State which cell type is depicted.
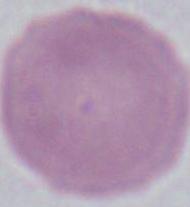

This is an erythrocyte.

Summary:
  - Modality: photomicrograph
  - Magnification: 1000x